Classify this cell by malaria status.
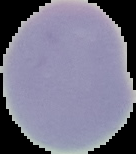
Uninfected.

Summary:
  - Image size: 136×154 pixels
  - Preparation: thin blood film
  - Image type: segmented cell region on a black background